Describe the morphology of the red blood cells.
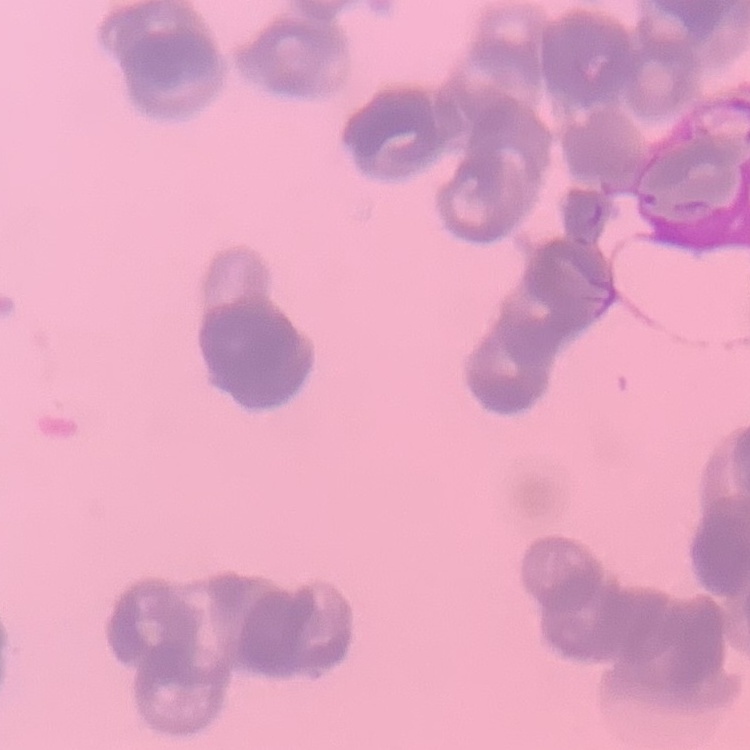

They show rouleaux formation.

Stained with either Field's or Giemsa. Thin peripheral smear. One tile cut from a larger photomicrograph.